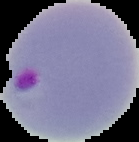
Summary:
  - Malaria status: parasitized
  - Preparation: thin blood film
  - Image size: 139×142 pixels
  - Image type: segmented cell region on a black background